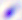

Micrograph. Toxoplasma gondii is shown. Captured at 400x magnification.